Locate every leukocyte (white blood cell).
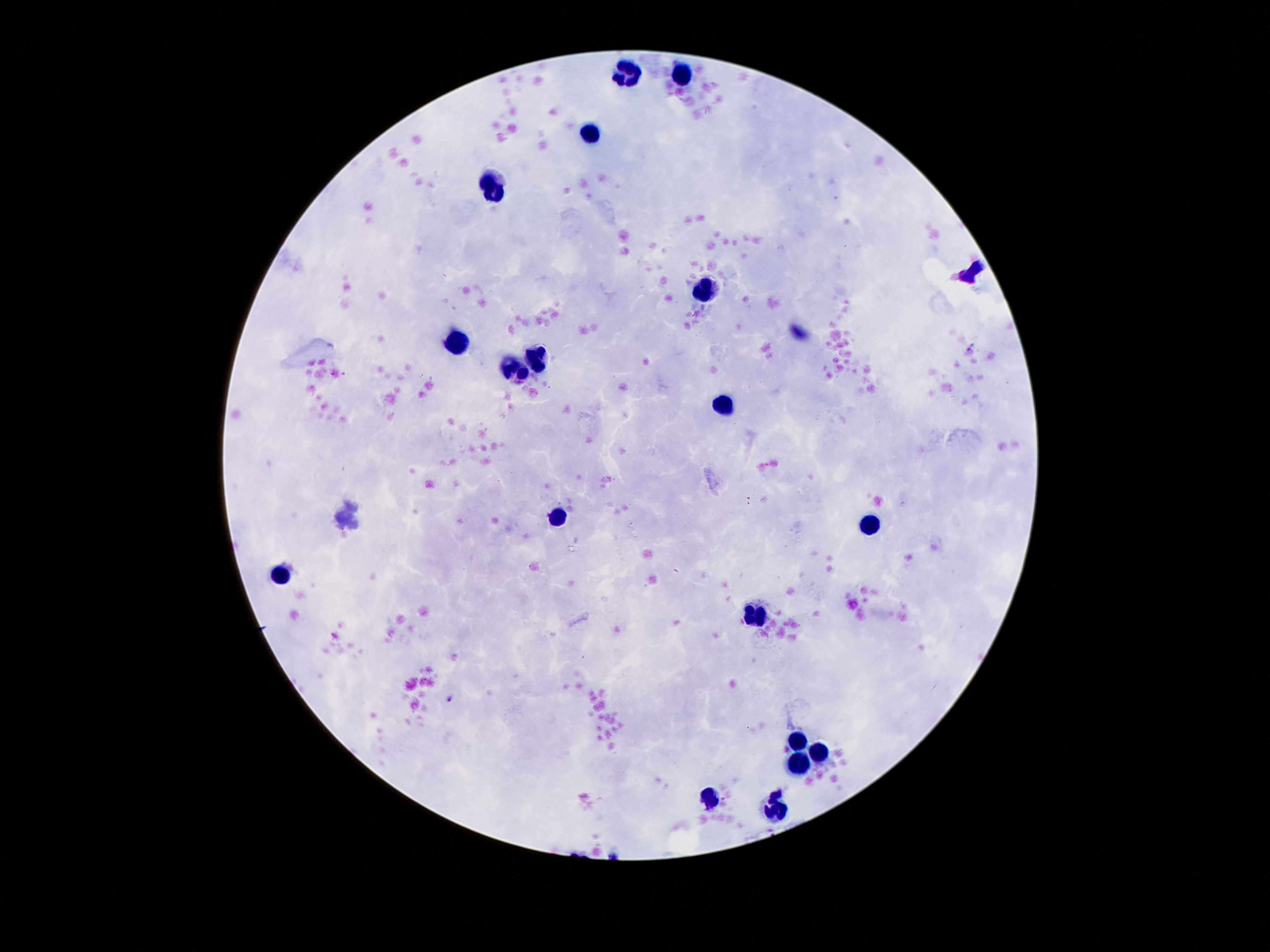
Approximate centers as {x, y} in pixels.
Leukocytes: {628, 74}, {685, 74}, {591, 133}, {491, 187}, {703, 292}, {457, 341}, {535, 357}, {514, 369}, {721, 407}, {562, 517}, {869, 525}, {282, 573}, {755, 619}, {798, 740}, {821, 752}, {794, 765}, {709, 799}, {773, 806}.

Summary:
  - Magnification: 100x
  - Patient malaria status: negative
  - Stain: Giemsa
  - Capture: smartphone camera through the microscope eyepiece
  - Field of view: one from this slide
  - Preparation: thick blood smear
  - Image size: 1270×952 pixels